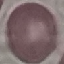
Summary:
  - Result: no malaria parasites detected
  - Capture: smartphone camera at the microscope eyepiece
  - Preparation: thin smear
  - Stain: Giemsa
  - Image type: automatically extracted cell patch, resized to 64 × 64 pixels